Classify this cell by malaria status.
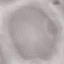

It is uninfected.

capture = smartphone camera at the microscope eyepiece
image type = cell patch, automatically extracted from a larger field of view and resized to 64 × 64 pixels
preparation = thin smear
stain = Giemsa